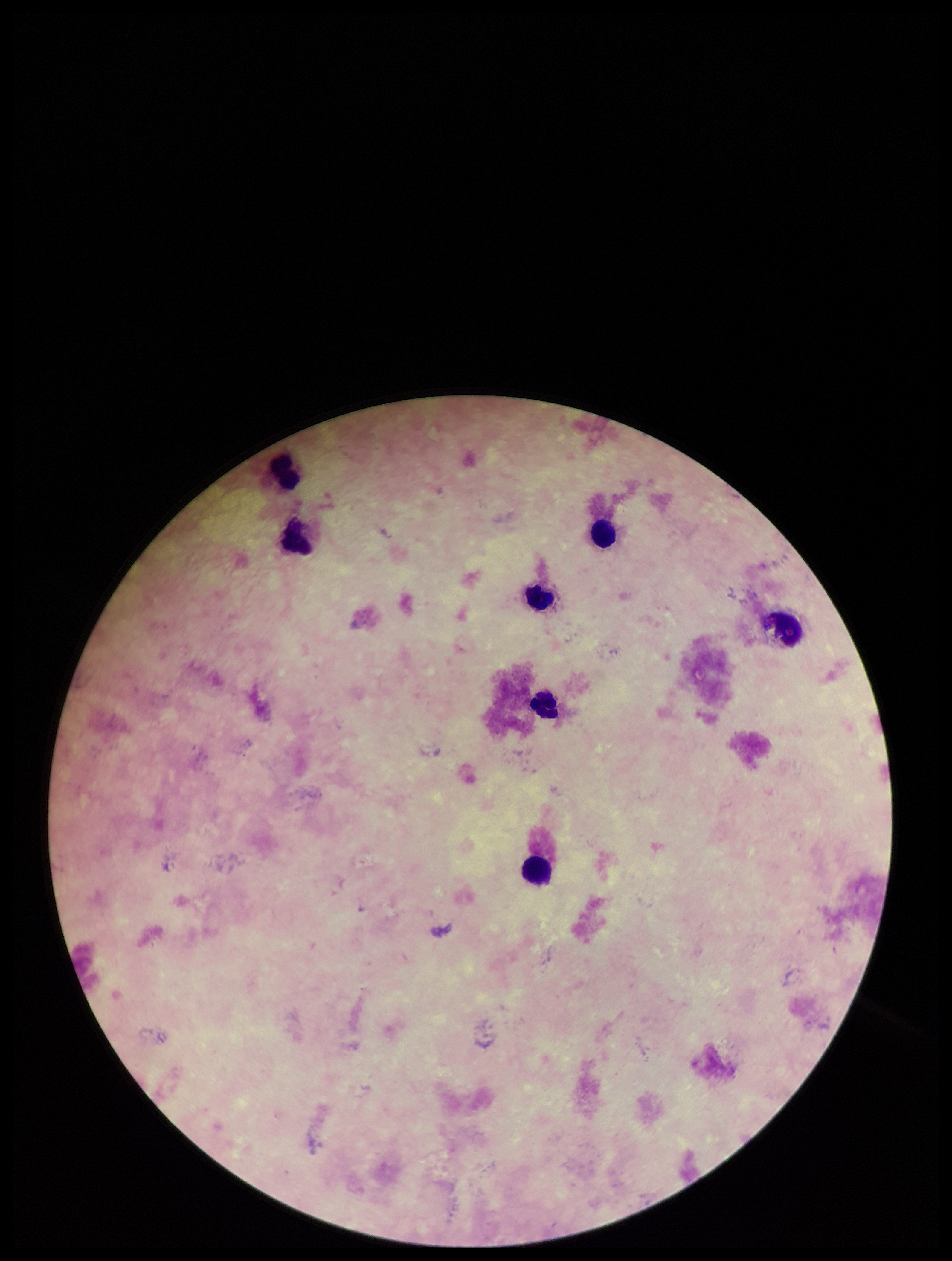

patient malaria status = negative
preparation = thick blood smear
image size = 952×1261 pixels
leukocyte count = 7
capture = smartphone photograph through the microscope eyepiece
field of view = single
parasite count = 0
Plasmodium parasites = none seen
stain = Giemsa